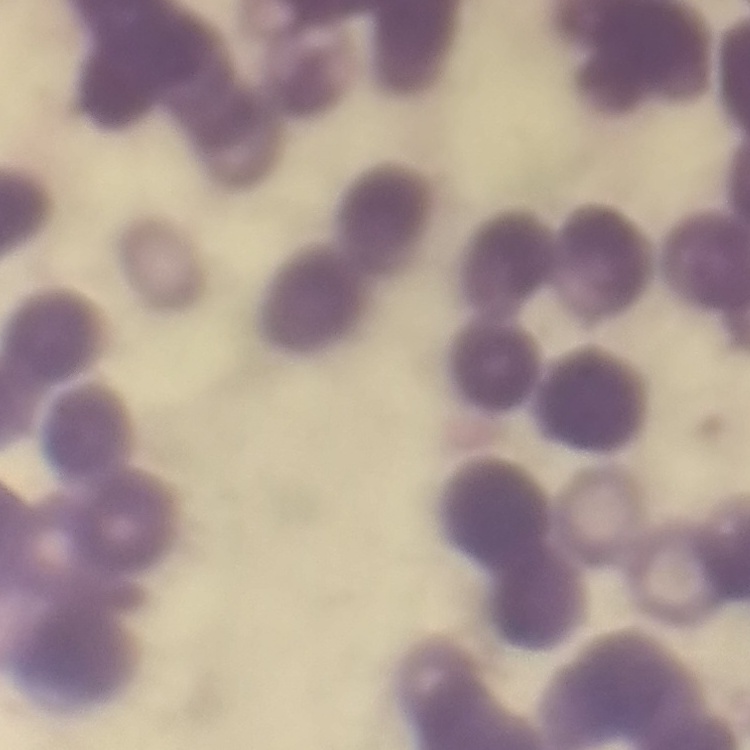
Summary:
  - Red blood cell morphology: rouleaux formation
  - Image type: square crop of a larger photomicrograph
  - Stain: Field's or Giemsa
  - Preparation: thin blood smear